Locate every Plasmodium parasite.
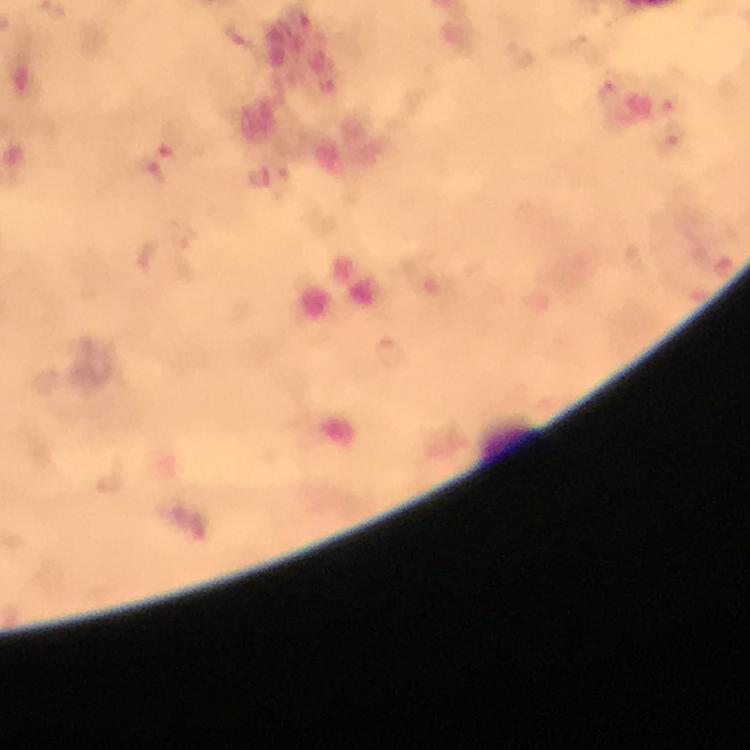

Approximate centers as [x, y] in pixels.
Plasmodium parasites (list possibly incomplete): [168, 145], [148, 170].

Summary:
  - Preparation: thick blood film
  - Immersion oil: used
  - Context: from a diagnostic examination for malaria
  - Stain: Giemsa
  - Cropped from: one field of view
  - Magnification: 100x
  - Capture: smartphone photograph through a microscope
  - Image size: 750×750 pixels